Report the malaria status of this cell.
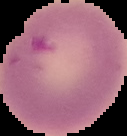

It is uninfected.

{
  "image_size": "127×136 pixels",
  "preparation": "thin blood film",
  "image_type": "cell region segmented out of the field of view; surrounding area masked to black"
}